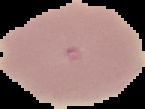

image size = 145×109 pixels
preparation = thin blood film
image type = segmented cell region with the area outside set to black
result = no Plasmodium parasites seen